Name the blood parasite species.
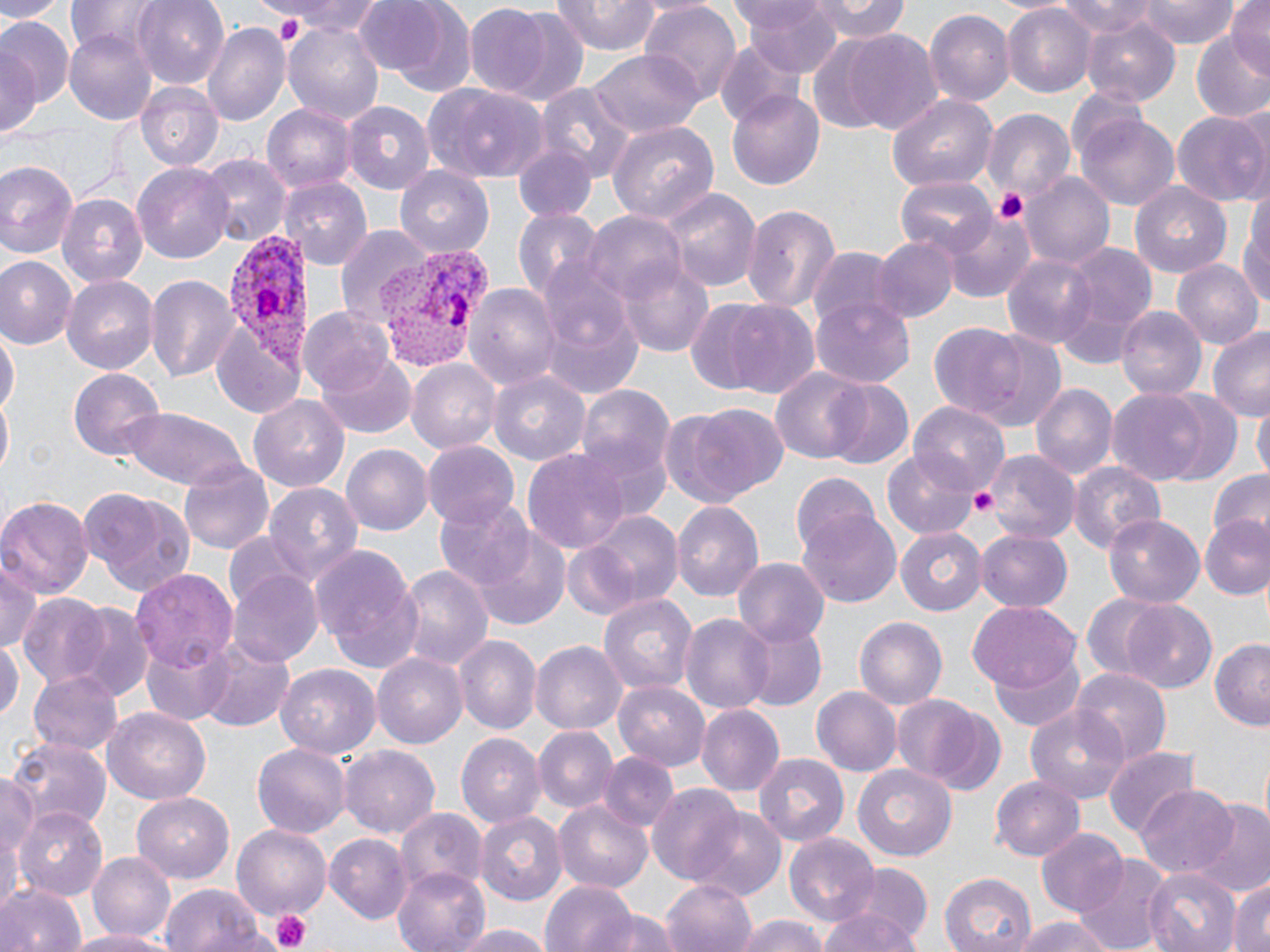

Plasmodium vivax.

{
  "uninfected_red_blood_cell_locations": "approximate bounding boxes as [x1, y1, x2, y2] in pixels: [0, 0, 62, 22], [133, 0, 230, 88], [356, 0, 453, 77], [742, 0, 841, 75], [806, 0, 910, 43], [1134, 0, 1241, 47], [1229, 0, 1270, 76], [256, 1, 388, 37], [554, 1, 661, 57], [1050, 1, 1163, 41], [638, 4, 743, 106], [388, 5, 479, 100], [476, 5, 590, 103], [1002, 6, 1094, 97], [928, 9, 1014, 107], [0, 14, 69, 125], [1080, 14, 1182, 107], [285, 22, 387, 123], [204, 23, 290, 127], [1191, 26, 1270, 126], [64, 30, 157, 123], [844, 31, 944, 134], [1, 33, 43, 148], [715, 38, 801, 126], [590, 52, 704, 136], [137, 82, 224, 171], [537, 82, 634, 178], [423, 83, 548, 183], [727, 89, 824, 192], [888, 95, 995, 191], [342, 100, 434, 195], [262, 104, 356, 194], [982, 108, 1075, 205], [1171, 112, 1269, 204], [1078, 116, 1178, 211], [606, 119, 718, 227], [513, 146, 595, 221], [201, 156, 288, 246], [0, 158, 81, 263], [133, 162, 235, 264], [393, 166, 497, 257], [1025, 173, 1115, 268], [896, 176, 997, 258], [280, 177, 371, 269], [1130, 178, 1232, 277], [659, 188, 759, 290], [1241, 191, 1269, 315], [57, 192, 145, 287], [739, 201, 843, 313], [513, 208, 600, 298], [946, 210, 1036, 301], [585, 213, 688, 308], [336, 224, 429, 325], [870, 235, 957, 324], [1053, 240, 1160, 362], [809, 247, 900, 331], [1001, 252, 1095, 348], [0, 254, 77, 349], [619, 257, 715, 357], [1171, 260, 1260, 350], [143, 271, 239, 384], [63, 273, 160, 372], [465, 279, 563, 391], [810, 296, 914, 388], [716, 300, 822, 398], [1117, 305, 1206, 401], [298, 306, 393, 398], [543, 309, 644, 396], [931, 319, 1064, 429], [1208, 326, 1270, 419], [1, 328, 17, 425], [319, 350, 415, 439], [407, 360, 498, 455], [68, 368, 168, 461], [772, 368, 870, 463], [488, 370, 592, 466], [819, 379, 915, 471], [1029, 382, 1115, 484], [576, 385, 676, 488], [1108, 390, 1211, 484], [1151, 390, 1246, 487], [250, 394, 348, 494], [0, 399, 11, 481], [1253, 399, 1268, 486], [670, 404, 785, 509], [911, 404, 1010, 499], [118, 406, 250, 491], [422, 441, 519, 530], [341, 445, 433, 536], [522, 449, 632, 558], [983, 450, 1081, 544], [885, 451, 977, 539], [178, 457, 274, 556], [1069, 460, 1166, 553], [789, 471, 879, 557], [1205, 471, 1270, 546], [263, 483, 363, 585], [78, 489, 195, 597], [0, 495, 94, 600], [434, 499, 539, 595], [673, 501, 764, 605], [576, 510, 686, 612], [799, 513, 901, 608], [1103, 513, 1205, 607], [1202, 514, 1269, 600], [468, 528, 573, 629], [896, 528, 986, 614], [977, 531, 1072, 612], [557, 535, 653, 619], [312, 545, 423, 672], [1, 557, 41, 655], [732, 557, 830, 647], [393, 564, 492, 673], [130, 567, 239, 670], [229, 568, 324, 668], [15, 593, 118, 691], [600, 593, 697, 700], [1081, 596, 1186, 690], [1119, 600, 1219, 695], [55, 601, 155, 702], [969, 601, 1080, 690], [680, 613, 773, 715], [854, 616, 947, 707], [737, 619, 825, 712], [139, 634, 234, 725], [0, 635, 22, 725], [455, 635, 540, 734], [1208, 639, 1270, 731], [199, 641, 292, 732], [532, 641, 625, 734], [990, 651, 1087, 732], [372, 652, 468, 747], [276, 665, 378, 762], [1070, 666, 1172, 766], [27, 670, 122, 757], [612, 680, 711, 769], [812, 685, 900, 777], [893, 695, 993, 789], [1025, 703, 1133, 803], [695, 704, 783, 799], [101, 706, 211, 805], [536, 727, 615, 814], [455, 732, 546, 829], [3, 737, 110, 835], [251, 742, 351, 837], [341, 745, 439, 839], [1103, 746, 1201, 837], [599, 753, 680, 835], [755, 755, 849, 848], [853, 764, 958, 862], [1, 772, 39, 894], [991, 774, 1085, 860], [646, 784, 747, 886], [1136, 786, 1239, 879], [134, 793, 233, 884], [553, 800, 655, 893], [1190, 802, 1270, 896], [14, 807, 109, 901], [686, 807, 786, 903], [396, 808, 486, 894], [476, 811, 566, 906], [233, 826, 330, 916], [1036, 827, 1125, 914], [328, 834, 413, 922], [785, 834, 882, 925], [88, 851, 176, 942], [1071, 852, 1173, 952], [392, 865, 493, 952], [1145, 868, 1239, 952], [1184, 871, 1270, 952], [940, 872, 1036, 952], [832, 873, 934, 952], [659, 879, 758, 952], [1230, 879, 1270, 952], [542, 880, 639, 952], [0, 881, 86, 952], [160, 884, 262, 952], [596, 908, 681, 952], [819, 909, 919, 952], [734, 915, 829, 952], [1014, 915, 1118, 952], [449, 923, 555, 952], [63, 930, 179, 952]",
  "platelet_locations": "approximate bounding boxes as [x1, y1, x2, y2] in pixels: [990, 188, 1032, 226], [967, 484, 998, 519], [265, 910, 313, 952]",
  "preparation": "thin blood smear",
  "stain": "May-Grünwald-Giemsa",
  "magnification": "1000x",
  "image_size": "1270×952 pixels",
  "field_of_view": "one of a larger specimen",
  "plasmodium_vivax_infected_red_blood_cell_locations": "approximate bounding boxes as [x1, y1, x2, y2] in pixels: [219, 222, 314, 394], [376, 246, 486, 369]",
  "modality": "light microscopy"
}